Assess the morphology of the red blood cells.
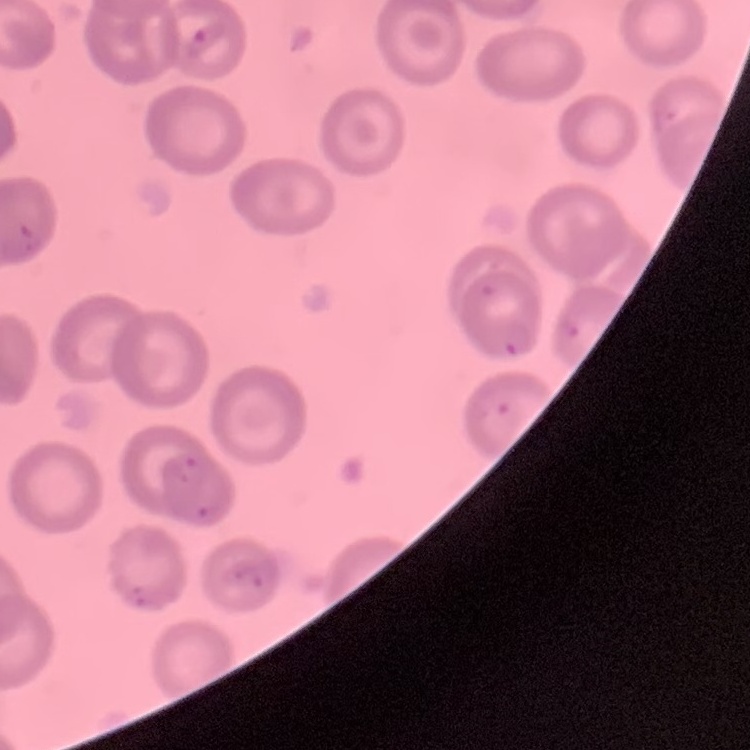

No rouleaux formation.

Field's or Giemsa stain. One tile cut from a larger photomicrograph. Thin blood film.